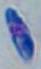
Summary:
  - Modality: photomicrograph
  - Magnification: 1000x
  - Identification: Toxoplasma gondii